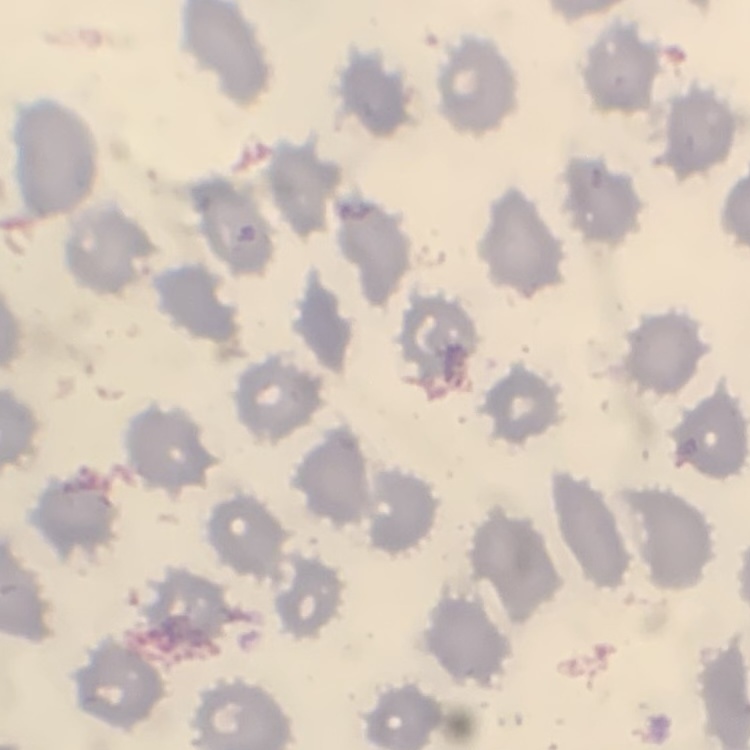
red blood cell morphology = no rouleaux formation
preparation = thin blood film
stain = Field's or Giemsa
image type = square crop of a larger photomicrograph